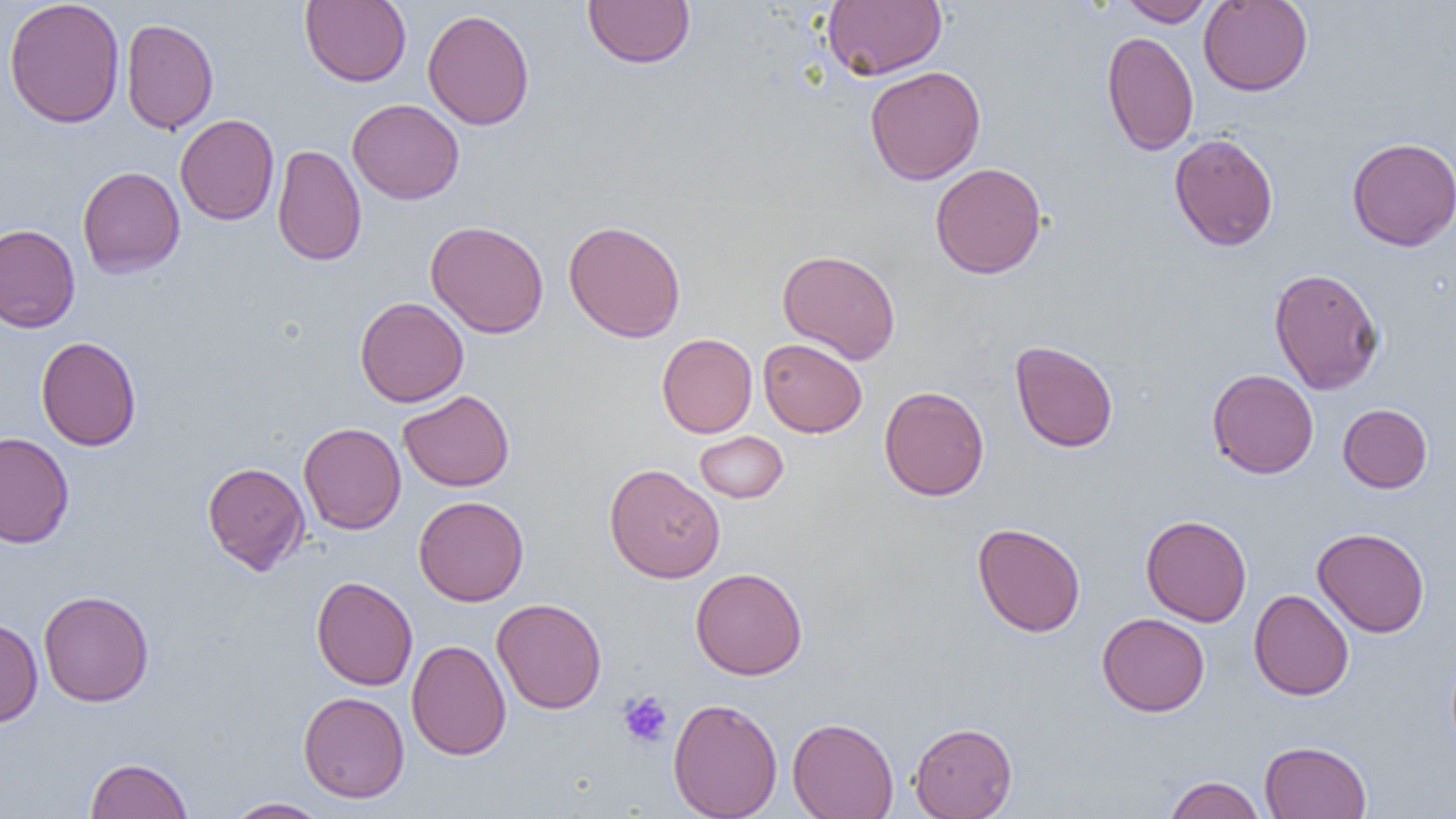

Summary:
  - Coordinate format: approximate bounding boxes as named x1/y1/x2/y2 corners in pixels
  - Uninfected red blood cell locations: (x1=3, y1=0, x2=125, y2=128), (x1=299, y1=0, x2=411, y2=87), (x1=583, y1=0, x2=695, y2=68), (x1=822, y1=0, x2=947, y2=80), (x1=1119, y1=0, x2=1213, y2=26), (x1=1198, y1=0, x2=1313, y2=96), (x1=422, y1=9, x2=535, y2=131), (x1=120, y1=17, x2=219, y2=134), (x1=1101, y1=31, x2=1199, y2=156), (x1=864, y1=66, x2=986, y2=185), (x1=347, y1=99, x2=464, y2=204), (x1=175, y1=114, x2=280, y2=225), (x1=1169, y1=133, x2=1279, y2=251), (x1=1346, y1=137, x2=1456, y2=251), (x1=273, y1=144, x2=366, y2=266), (x1=930, y1=162, x2=1047, y2=279), (x1=77, y1=166, x2=185, y2=278), (x1=426, y1=220, x2=550, y2=338), (x1=563, y1=220, x2=687, y2=343), (x1=0, y1=224, x2=81, y2=333), (x1=776, y1=248, x2=901, y2=364), (x1=1268, y1=267, x2=1384, y2=395), (x1=355, y1=297, x2=469, y2=406), (x1=657, y1=333, x2=757, y2=438), (x1=36, y1=336, x2=141, y2=451), (x1=758, y1=338, x2=868, y2=438), (x1=1009, y1=340, x2=1119, y2=453), (x1=1207, y1=369, x2=1319, y2=478), (x1=879, y1=386, x2=989, y2=501), (x1=398, y1=390, x2=514, y2=492), (x1=1338, y1=403, x2=1433, y2=493), (x1=299, y1=422, x2=406, y2=535), (x1=694, y1=431, x2=789, y2=504), (x1=0, y1=432, x2=74, y2=548), (x1=202, y1=461, x2=311, y2=575), (x1=604, y1=463, x2=725, y2=583), (x1=413, y1=496, x2=529, y2=606), (x1=1141, y1=515, x2=1252, y2=626), (x1=972, y1=522, x2=1086, y2=637), (x1=1312, y1=527, x2=1430, y2=637), (x1=690, y1=567, x2=808, y2=680), (x1=311, y1=575, x2=418, y2=690), (x1=1249, y1=589, x2=1354, y2=700), (x1=38, y1=590, x2=154, y2=707), (x1=491, y1=598, x2=607, y2=714), (x1=1097, y1=612, x2=1210, y2=717), (x1=0, y1=618, x2=43, y2=727), (x1=407, y1=639, x2=511, y2=760), (x1=298, y1=691, x2=410, y2=803), (x1=667, y1=697, x2=783, y2=819), (x1=787, y1=716, x2=899, y2=819), (x1=909, y1=721, x2=1017, y2=818), (x1=1259, y1=740, x2=1372, y2=819), (x1=85, y1=757, x2=193, y2=818), (x1=1163, y1=775, x2=1266, y2=818), (x1=223, y1=797, x2=333, y2=818)
  - Platelet locations: (x1=618, y1=690, x2=674, y2=749)
  - Slide-level diagnosis: negative for blood parasites
  - Field of view: single
  - Preparation: thin blood smear
  - Image size: 1456×819 pixels
  - Magnification: 1000x
  - Modality: light microscopy